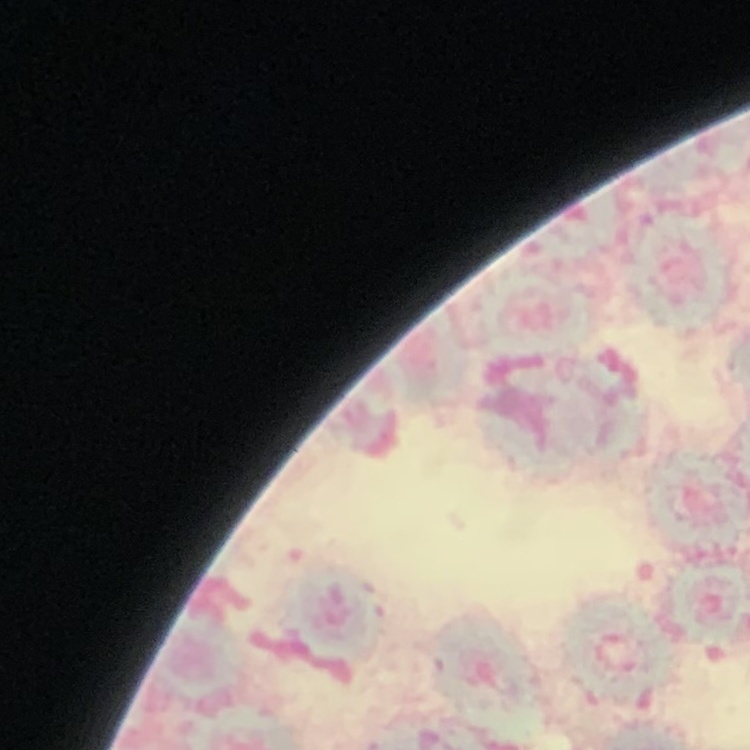

erythrocyte morphology = rouleaux formation
stain = Field's or Giemsa
preparation = thin blood smear
image type = square crop of a larger photomicrograph